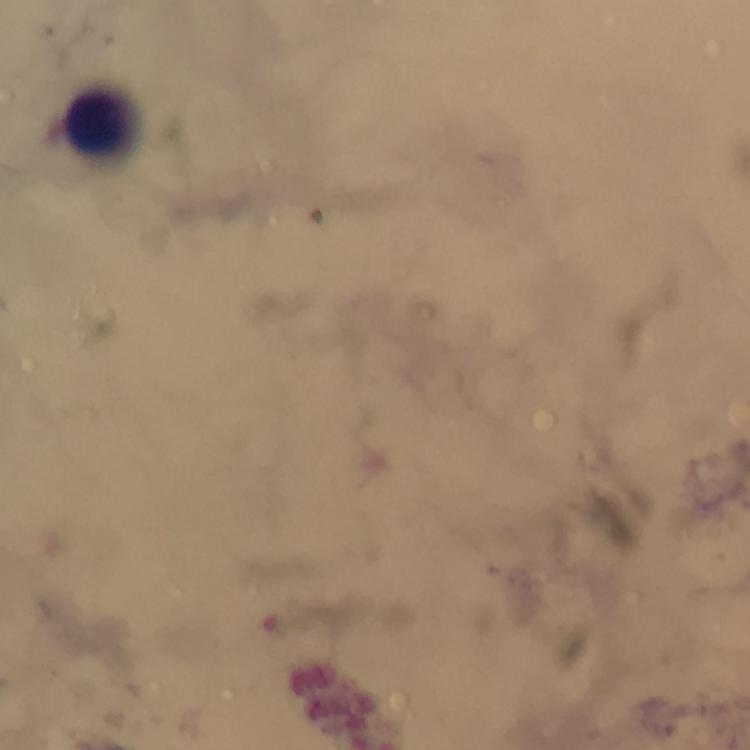

{
  "cropped_from": "a single field of view",
  "magnification": "100x",
  "image_size": "750×750 pixels",
  "immersion_oil": "used",
  "stain": "Giemsa",
  "plasmodium_parasites": "none seen",
  "capture": "smartphone camera through the microscope",
  "preparation": "thick blood smear",
  "leukocyte_locations": "approximate centers as (x, y) in pixels: (97, 121)",
  "context": "from a malaria diagnostic workup"
}